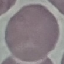

Summary:
  - Result: no malaria parasites detected
  - Stain: Giemsa
  - Preparation: thin blood smear
  - Image type: cell patch, automatically extracted from a larger field of view and resized to 64 × 64 pixels
  - Capture: smartphone through the microscope eyepiece